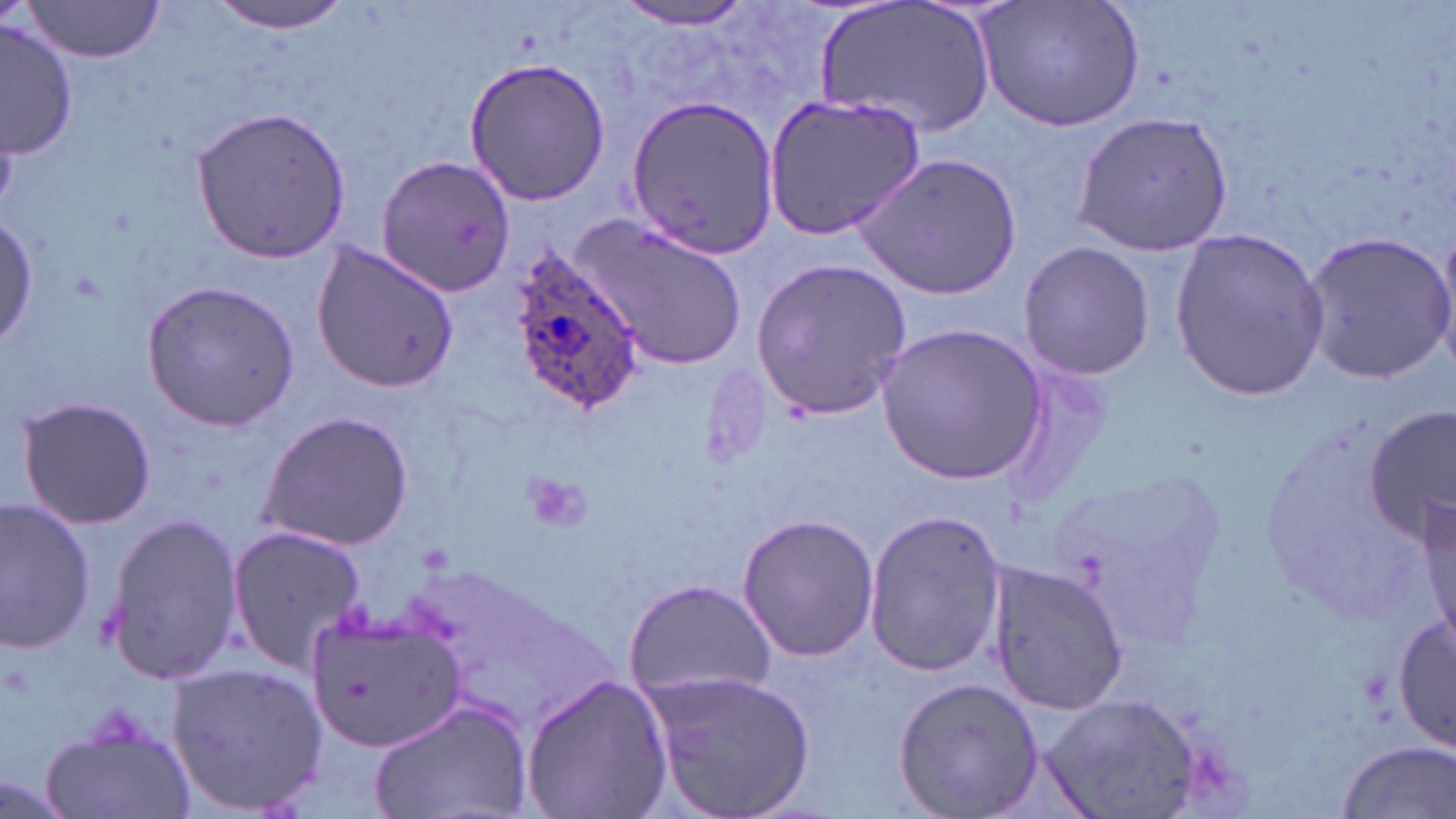

slide-level diagnosis = Plasmodium ovale
image size = 1456×819 pixels
magnification = 1000x
uninfected red blood cell locations = approximate bounding boxes as [x1, y1, x2, y2] in pixels: [17, 0, 166, 62], [207, 0, 355, 34], [814, 0, 996, 139], [976, 0, 1145, 132], [612, 2, 760, 29], [2, 20, 78, 159], [461, 56, 612, 206], [625, 93, 780, 260], [762, 94, 926, 238], [188, 106, 351, 264], [1071, 110, 1234, 256], [854, 152, 1022, 302], [376, 154, 516, 298], [0, 207, 45, 356], [577, 214, 748, 370], [1299, 227, 1453, 380], [1168, 229, 1330, 401], [1019, 239, 1153, 381], [310, 240, 460, 391], [750, 255, 913, 423], [139, 278, 302, 433], [878, 323, 1047, 483], [13, 395, 156, 530], [1366, 407, 1455, 544], [256, 410, 415, 550], [1421, 491, 1455, 650], [0, 497, 98, 655], [862, 508, 1008, 679], [736, 511, 881, 664], [103, 512, 242, 686], [225, 521, 367, 672], [985, 559, 1131, 717], [624, 577, 778, 703], [303, 606, 463, 755], [1392, 612, 1456, 751], [165, 661, 330, 815], [645, 667, 818, 819], [518, 671, 673, 819], [891, 676, 1044, 819], [1034, 692, 1218, 819], [371, 698, 531, 819], [42, 711, 198, 819], [1335, 740, 1454, 818]
field of view = single
stain = May-Grünwald-Giemsa
platelet locations = approximate bounding boxes as [x1, y1, x2, y2] in pixels: [524, 472, 593, 534]
Plasmodium ovale-infected red blood cell locations = approximate bounding boxes as [x1, y1, x2, y2] in pixels: [508, 249, 643, 416]
preparation = thin blood smear
modality = light microscopy